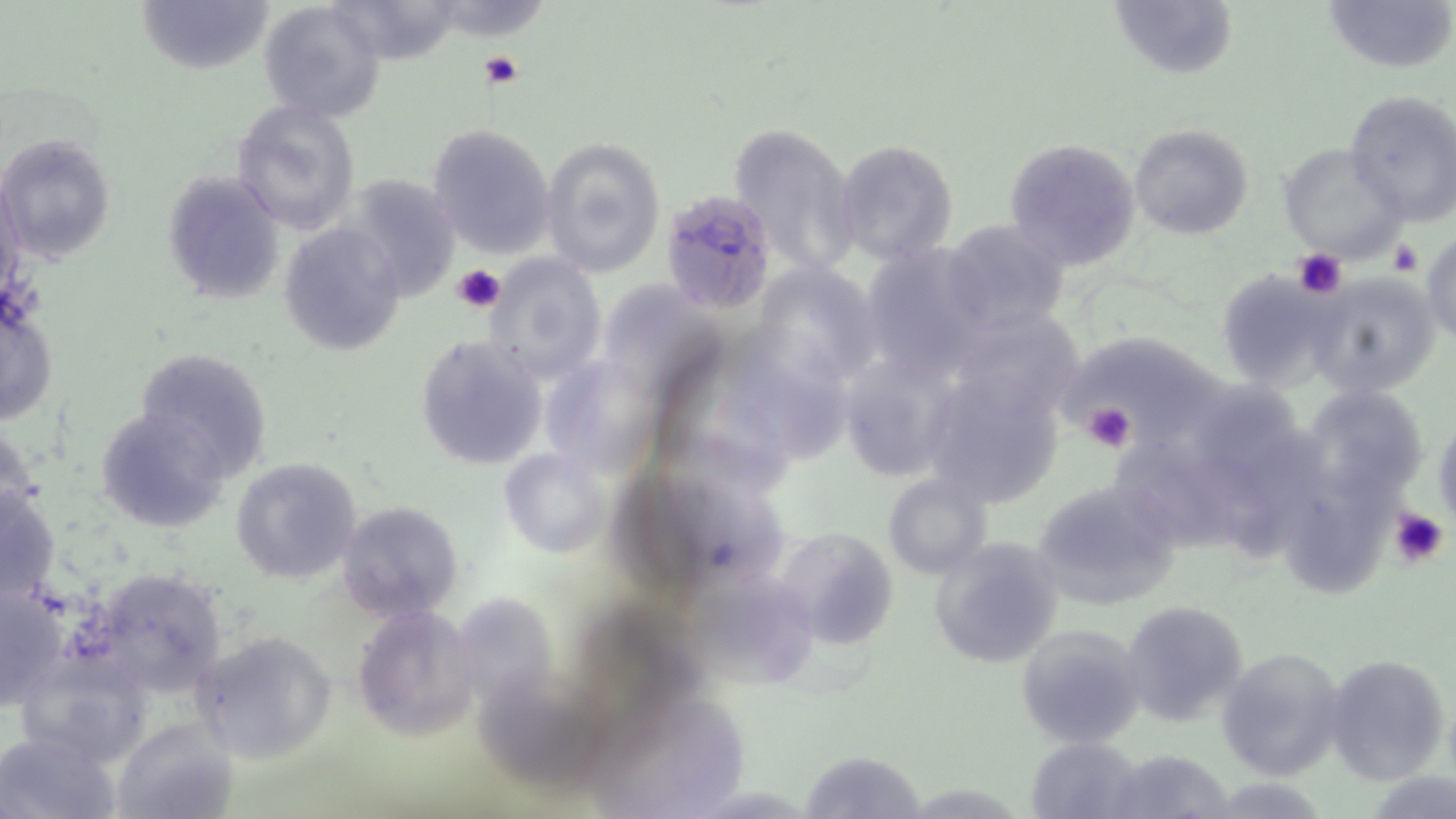

Summary:
  - Coordinate format: approximate bounding boxes as (x1,y1)-(x2,y2) corner pairs in pixels
  - Platelet locations: (481,50)-(526,90), (1388,239)-(1422,276), (1292,248)-(1349,299), (452,264)-(506,313), (1081,400)-(1138,453), (1430,426)-(1455,525), (1388,507)-(1451,571)
  - Plasmodium falciparum-infected red blood cell locations: (658,189)-(775,314)
  - Uninfected red blood cell locations: (137,0)-(272,76), (330,0)-(464,65), (1109,0)-(1237,81), (1323,0)-(1453,76), (256,2)-(387,123), (1343,90)-(1456,225), (231,98)-(362,235), (725,121)-(861,276), (426,123)-(555,258), (1128,123)-(1254,241), (0,132)-(117,264), (540,136)-(666,278), (832,138)-(959,268), (1003,138)-(1140,272), (1276,143)-(1406,263), (161,172)-(286,304), (340,173)-(462,302), (940,217)-(1070,337), (278,221)-(407,353), (1422,231)-(1455,348), (860,243)-(992,379), (481,253)-(608,383), (765,259)-(894,389), (1216,269)-(1338,388), (1307,272)-(1441,399), (611,284)-(735,424), (0,303)-(59,423), (965,310)-(1099,430), (735,327)-(858,458), (414,334)-(549,469), (1072,335)-(1243,457), (132,346)-(273,482), (918,359)-(1067,505), (540,364)-(662,484), (1189,370)-(1299,512), (1307,387)-(1426,517), (660,395)-(800,509), (94,405)-(231,532), (1433,410)-(1455,530), (1228,421)-(1341,566), (1117,445)-(1245,558), (498,447)-(610,560), (230,457)-(364,585), (884,472)-(994,579), (650,474)-(802,598), (1030,477)-(1181,608), (0,482)-(61,606), (1294,485)-(1401,602), (336,501)-(463,624), (773,523)-(902,649), (926,536)-(1066,671), (84,566)-(231,699), (1,584)-(69,709), (701,584)-(826,692), (457,586)-(560,724), (1120,599)-(1252,727), (350,602)-(482,742), (586,604)-(715,725), (1014,624)-(1145,748), (192,630)-(338,764), (1215,645)-(1348,782), (1324,653)-(1452,784), (487,676)-(611,788), (114,719)-(234,816), (0,730)-(118,818), (1025,736)-(1141,817), (1105,748)-(1235,818), (799,749)-(922,817)
  - Slide-level diagnosis: Plasmodium falciparum
  - Magnification: 1000x
  - Stain: May-Grünwald-Giemsa
  - Image size: 1456×819 pixels
  - Field of view: one of a larger specimen
  - Modality: light microscopy
  - Preparation: thin blood smear